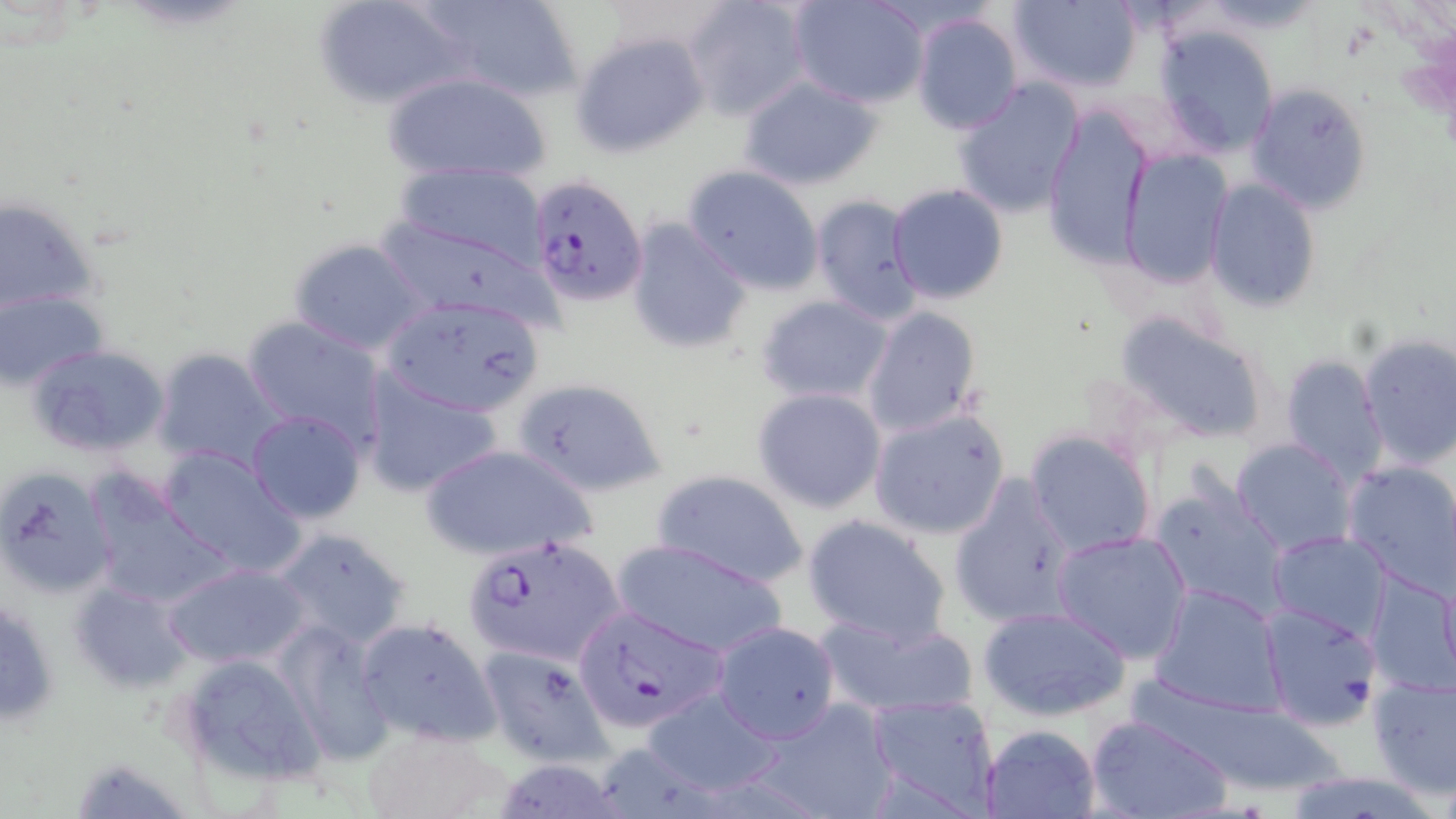

Summary:
  - Coordinate format: approximate bounding boxes as (x1,y1)-(x2,y2) corner pairs in pixels
  - Uninfected red blood cell locations: (313,0)-(469,109), (423,0)-(581,104), (684,0)-(809,121), (788,0)-(929,107), (1007,0)-(1143,92), (1186,1)-(1330,34), (910,11)-(1025,136), (1154,26)-(1280,156), (573,32)-(708,156), (382,71)-(552,186), (736,73)-(885,191), (950,77)-(1085,220), (1245,82)-(1372,215), (1041,106)-(1154,268), (1118,149)-(1234,290), (394,162)-(550,270), (683,164)-(825,294), (1205,179)-(1322,312), (887,183)-(1010,304), (809,193)-(924,325), (1,194)-(101,319), (624,216)-(755,357), (373,218)-(553,327), (288,236)-(431,357), (1,289)-(108,389), (756,294)-(893,406), (379,295)-(544,417), (861,307)-(983,437), (1117,310)-(1272,444), (241,316)-(390,450), (1355,333)-(1456,471), (23,342)-(170,459), (150,349)-(282,472), (1278,354)-(1389,485), (361,374)-(505,496), (510,376)-(670,497), (752,386)-(888,514), (868,407)-(1011,540), (246,410)-(366,523), (1024,430)-(1158,558), (1231,437)-(1355,557), (247,440)-(389,613), (420,443)-(597,560), (156,446)-(307,575), (1342,460)-(1456,592), (0,465)-(116,598), (652,469)-(810,590), (949,475)-(1077,629), (86,478)-(234,610), (1148,480)-(1290,621), (802,514)-(953,648), (269,528)-(414,651), (1050,530)-(1193,664), (1268,531)-(1391,642), (609,537)-(790,660), (162,562)-(310,668), (1365,571)-(1456,700), (69,579)-(197,695), (1148,584)-(1287,717), (0,591)-(63,727), (1258,603)-(1382,727), (977,605)-(1133,722), (817,612)-(979,719), (353,615)-(501,749), (276,620)-(397,765), (711,621)-(841,742), (479,643)-(615,769), (171,651)-(326,790), (1366,676)-(1456,801), (640,687)-(785,797), (865,695)-(1002,815), (749,698)-(901,818), (1084,714)-(1232,819), (980,724)-(1101,819), (358,726)-(506,819), (68,754)-(195,817), (1279,770)-(1445,819)
  - Plasmodium falciparum-infected red blood cell locations: (529,174)-(648,307), (461,533)-(628,669), (573,606)-(727,733)
  - Slide-level diagnosis: Plasmodium falciparum
  - Magnification: 1000x
  - Field of view: one of a larger specimen
  - Image size: 1456×819 pixels
  - Modality: light microscopy
  - Preparation: thin blood film
  - Stain: May-Grünwald-Giemsa